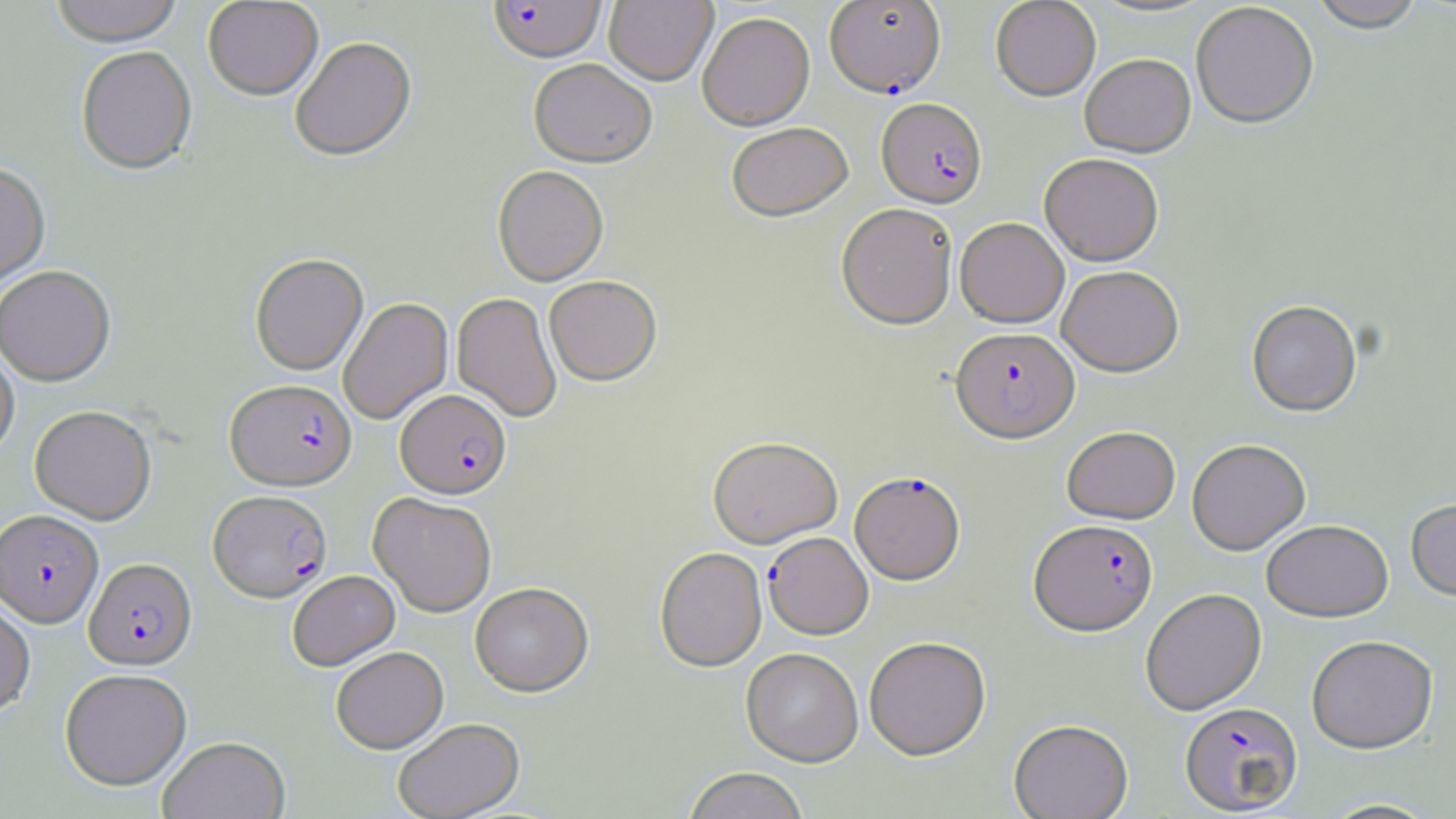

slide-level diagnosis = Plasmodium falciparum
field of view = single
stain = May-Grünwald-Giemsa
uninfected red blood cell locations = approximate bounding boxes as [x1, y1, x2, y2] in pixels: [49, 0, 183, 50], [203, 0, 324, 103], [604, 0, 718, 88], [990, 0, 1101, 102], [1087, 0, 1218, 20], [1309, 0, 1425, 36], [1191, 4, 1318, 131], [697, 14, 815, 130], [290, 40, 417, 164], [76, 49, 197, 178], [1080, 55, 1196, 159], [528, 61, 656, 169], [727, 124, 854, 225], [1040, 155, 1163, 268], [0, 165, 51, 291], [492, 167, 609, 288], [836, 205, 958, 332], [955, 220, 1069, 329], [250, 254, 369, 377], [1057, 267, 1183, 378], [0, 268, 116, 388], [544, 276, 662, 387], [451, 293, 562, 423], [338, 297, 453, 425], [1247, 302, 1362, 418], [0, 347, 19, 463], [30, 407, 156, 525], [1062, 427, 1180, 525], [708, 438, 843, 550], [1187, 440, 1310, 557], [368, 493, 496, 618], [1405, 498, 1456, 603], [1262, 522, 1393, 624], [655, 549, 767, 673], [288, 571, 400, 672], [470, 584, 595, 698], [1140, 589, 1267, 715], [0, 597, 35, 719], [1306, 637, 1439, 756], [864, 638, 991, 763], [332, 647, 448, 755], [741, 650, 863, 768], [59, 669, 191, 791], [1009, 719, 1133, 819], [393, 720, 525, 819], [157, 736, 291, 819], [682, 769, 810, 819], [1318, 798, 1441, 818]
modality = light microscopy
magnification = 1000x
Plasmodium falciparum-infected red blood cell locations = approximate bounding boxes as [x1, y1, x2, y2] in pixels: [487, 1, 607, 66], [825, 1, 947, 99], [877, 100, 987, 210], [950, 329, 1080, 447], [225, 380, 356, 493], [395, 390, 512, 501], [849, 473, 966, 586], [208, 491, 332, 603], [0, 510, 104, 629], [1029, 520, 1158, 637], [762, 532, 873, 641], [84, 559, 197, 671], [1180, 702, 1303, 816]
image size = 1456×819 pixels
preparation = thin blood film